State the preparation type.
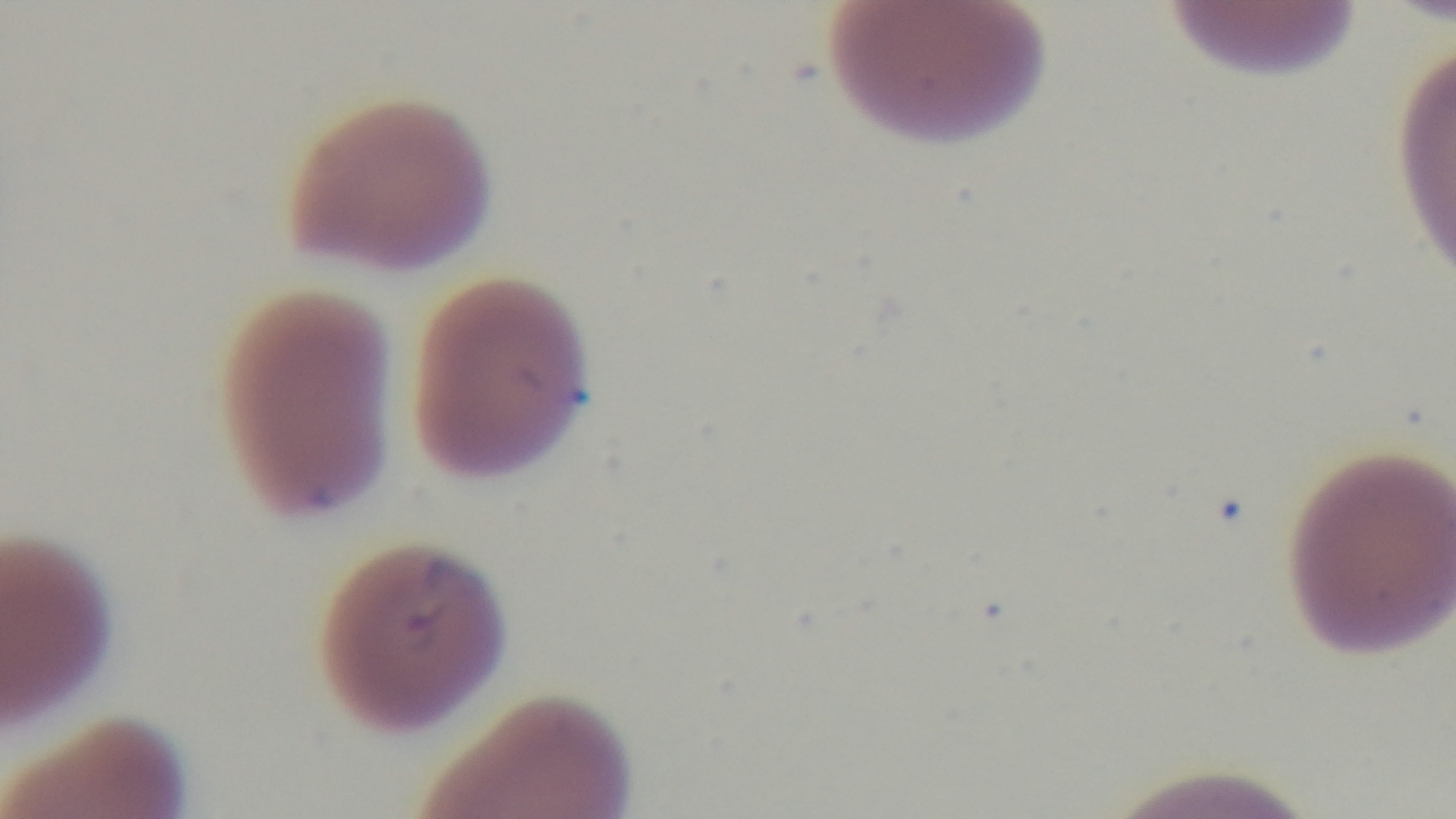

A thin smear.

capture: mounted 4K digital camera
stain: Giemsa
modality: light microscopy
objective: 100x oil immersion
field_of_view: one from the slide
malaria_status: infected